State which parasite is depicted.
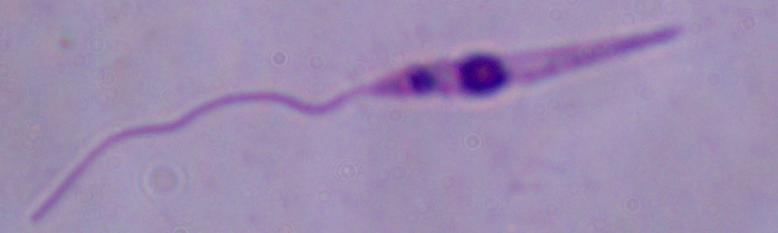
Leishmania.

Summary:
  - Magnification: 1000x
  - Modality: photomicrograph